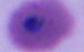 Micrograph. 400x or 1000x magnification. A Plasmodium parasite is seen.